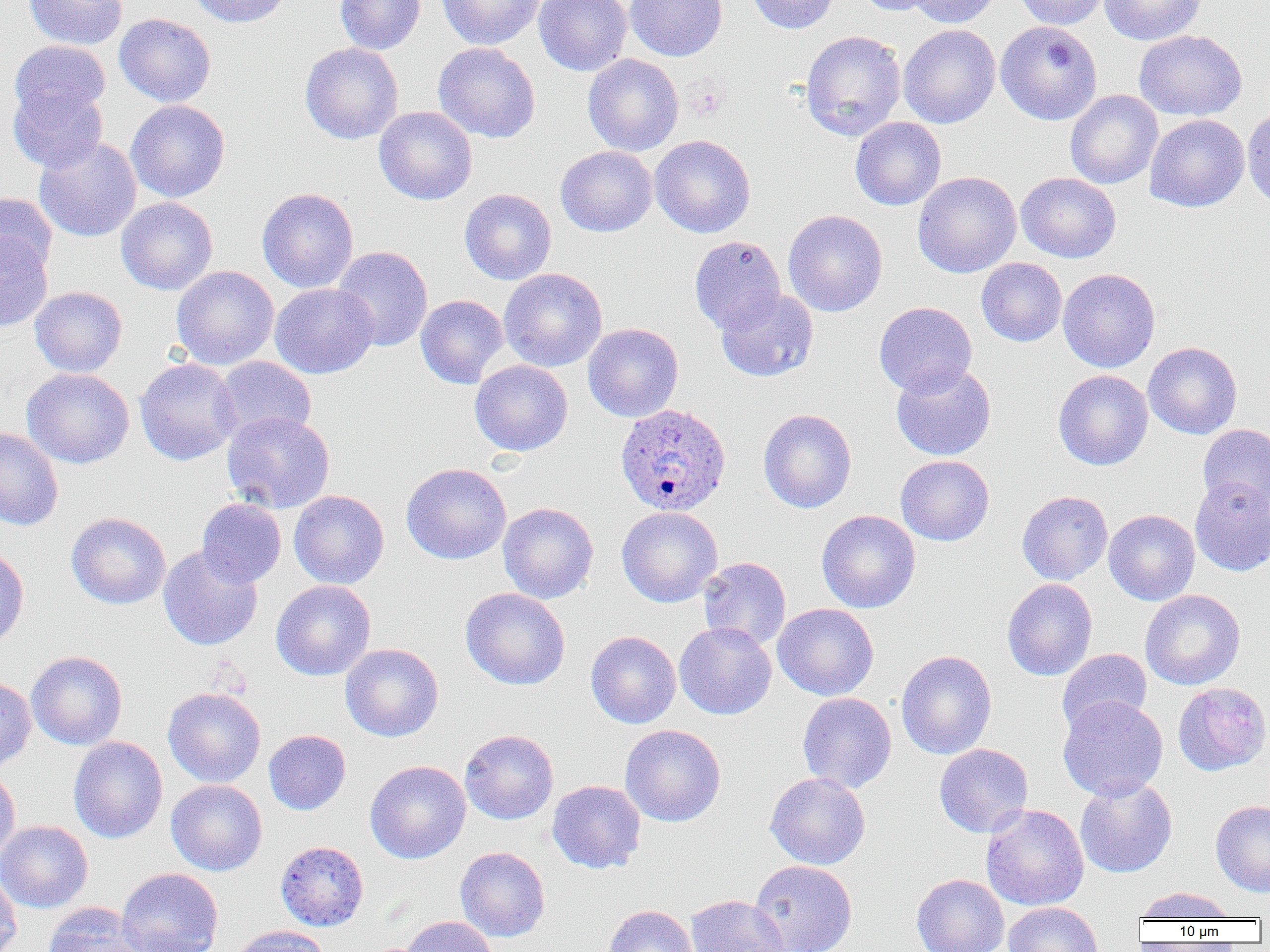
slide-level diagnosis = Plasmodium ovale
image size = 1270×952 pixels
Plasmodium ovale-infected red blood cell locations = approximate bounding boxes as named x1/y1/x2/y2 corners in pixels: (x1=615, y1=403, x2=731, y2=517)
modality = light microscopy
magnification = 1000x
field of view = single
preparation = thin blood film
platelet locations = approximate bounding boxes as named x1/y1/x2/y2 corners in pixels: (x1=684, y1=77, x2=728, y2=120)
uninfected red blood cell locations = approximate bounding boxes as named x1/y1/x2/y2 corners in pixels: (x1=24, y1=0, x2=128, y2=49), (x1=188, y1=0, x2=294, y2=28), (x1=335, y1=0, x2=425, y2=54), (x1=437, y1=0, x2=546, y2=50), (x1=534, y1=0, x2=632, y2=76), (x1=625, y1=0, x2=728, y2=61), (x1=746, y1=0, x2=839, y2=34), (x1=854, y1=0, x2=940, y2=16), (x1=906, y1=0, x2=1001, y2=27), (x1=1013, y1=0, x2=1108, y2=29), (x1=1099, y1=0, x2=1206, y2=45), (x1=115, y1=13, x2=216, y2=107), (x1=995, y1=20, x2=1102, y2=125), (x1=899, y1=24, x2=1001, y2=128), (x1=800, y1=29, x2=906, y2=140), (x1=1134, y1=30, x2=1247, y2=121), (x1=9, y1=40, x2=110, y2=123), (x1=300, y1=42, x2=403, y2=144), (x1=433, y1=42, x2=540, y2=143), (x1=583, y1=53, x2=683, y2=156), (x1=8, y1=80, x2=108, y2=173), (x1=1065, y1=90, x2=1163, y2=189), (x1=125, y1=99, x2=231, y2=202), (x1=1242, y1=105, x2=1270, y2=212), (x1=374, y1=106, x2=477, y2=205), (x1=1145, y1=114, x2=1249, y2=212), (x1=850, y1=117, x2=946, y2=210), (x1=650, y1=135, x2=756, y2=238), (x1=34, y1=136, x2=141, y2=242), (x1=556, y1=145, x2=657, y2=237), (x1=913, y1=171, x2=1021, y2=277), (x1=1016, y1=172, x2=1121, y2=263), (x1=257, y1=187, x2=358, y2=293), (x1=459, y1=188, x2=556, y2=285), (x1=0, y1=193, x2=56, y2=278), (x1=116, y1=197, x2=218, y2=295), (x1=782, y1=209, x2=887, y2=316), (x1=0, y1=232, x2=53, y2=332), (x1=689, y1=236, x2=786, y2=334), (x1=332, y1=246, x2=433, y2=352), (x1=976, y1=258, x2=1067, y2=346), (x1=171, y1=266, x2=279, y2=369), (x1=498, y1=268, x2=607, y2=371), (x1=1058, y1=268, x2=1160, y2=372), (x1=270, y1=283, x2=378, y2=378), (x1=30, y1=286, x2=127, y2=377), (x1=715, y1=289, x2=818, y2=382), (x1=415, y1=295, x2=509, y2=389), (x1=874, y1=301, x2=977, y2=396), (x1=583, y1=322, x2=684, y2=422), (x1=1143, y1=342, x2=1242, y2=439), (x1=214, y1=356, x2=316, y2=443), (x1=135, y1=357, x2=241, y2=466), (x1=469, y1=360, x2=573, y2=456), (x1=891, y1=362, x2=996, y2=461), (x1=21, y1=367, x2=134, y2=469), (x1=1053, y1=369, x2=1153, y2=471), (x1=758, y1=408, x2=857, y2=513), (x1=222, y1=411, x2=335, y2=514), (x1=1197, y1=424, x2=1270, y2=513), (x1=0, y1=428, x2=63, y2=530), (x1=896, y1=455, x2=994, y2=546), (x1=401, y1=462, x2=511, y2=564), (x1=1190, y1=476, x2=1270, y2=576), (x1=289, y1=490, x2=389, y2=589), (x1=1017, y1=490, x2=1113, y2=585), (x1=197, y1=498, x2=286, y2=587), (x1=497, y1=502, x2=599, y2=603), (x1=616, y1=506, x2=723, y2=607), (x1=816, y1=509, x2=920, y2=613), (x1=1103, y1=509, x2=1200, y2=605), (x1=66, y1=512, x2=171, y2=609), (x1=0, y1=545, x2=29, y2=649), (x1=158, y1=545, x2=263, y2=651), (x1=699, y1=557, x2=791, y2=650), (x1=1002, y1=578, x2=1097, y2=681), (x1=271, y1=580, x2=376, y2=681), (x1=460, y1=587, x2=570, y2=689), (x1=1140, y1=589, x2=1245, y2=690), (x1=772, y1=603, x2=879, y2=700), (x1=674, y1=621, x2=777, y2=719), (x1=586, y1=630, x2=681, y2=728), (x1=340, y1=643, x2=444, y2=742), (x1=1057, y1=649, x2=1152, y2=736), (x1=27, y1=650, x2=127, y2=750), (x1=895, y1=650, x2=996, y2=760), (x1=0, y1=677, x2=36, y2=773), (x1=1173, y1=682, x2=1270, y2=776), (x1=163, y1=687, x2=266, y2=787), (x1=797, y1=692, x2=897, y2=793), (x1=1057, y1=696, x2=1169, y2=800), (x1=620, y1=724, x2=726, y2=827), (x1=459, y1=729, x2=559, y2=824), (x1=264, y1=730, x2=351, y2=815), (x1=68, y1=736, x2=168, y2=843), (x1=934, y1=743, x2=1033, y2=837), (x1=365, y1=760, x2=471, y2=864), (x1=0, y1=767, x2=21, y2=865), (x1=765, y1=772, x2=871, y2=870), (x1=1075, y1=777, x2=1177, y2=879), (x1=166, y1=779, x2=267, y2=876), (x1=547, y1=780, x2=645, y2=873), (x1=1211, y1=800, x2=1270, y2=897), (x1=981, y1=804, x2=1089, y2=910), (x1=0, y1=820, x2=93, y2=913), (x1=275, y1=840, x2=369, y2=931), (x1=455, y1=846, x2=550, y2=942), (x1=749, y1=859, x2=858, y2=952), (x1=116, y1=868, x2=224, y2=952), (x1=0, y1=870, x2=22, y2=952), (x1=911, y1=874, x2=1009, y2=952), (x1=1134, y1=887, x2=1236, y2=923), (x1=684, y1=894, x2=790, y2=952), (x1=1003, y1=901, x2=1103, y2=952), (x1=42, y1=903, x2=147, y2=952), (x1=604, y1=904, x2=698, y2=952), (x1=398, y1=915, x2=498, y2=952), (x1=231, y1=925, x2=331, y2=952)